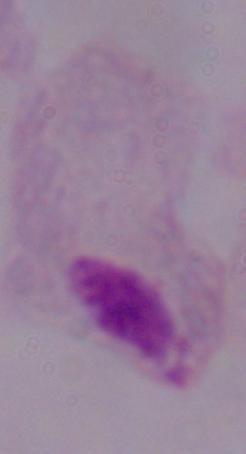
modality: micrograph
identification: trichomonad
magnification: 1000x